Identify the blood parasite species.
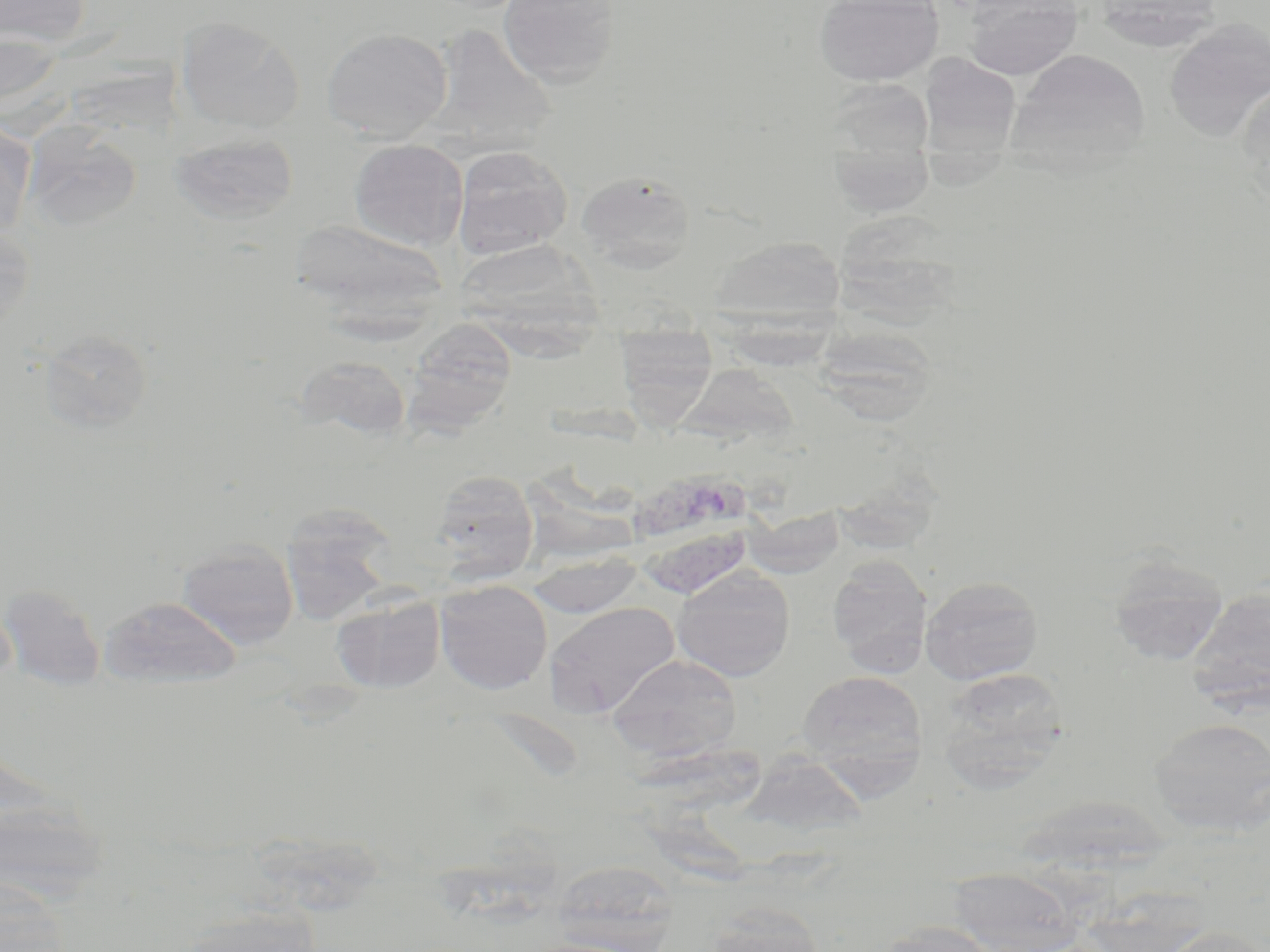

Plasmodium vivax.

{
  "field_of_view": "one of a larger specimen",
  "modality": "light microscopy",
  "stain": "May-Grünwald-Giemsa",
  "preparation": "thin blood smear",
  "uninfected_red_blood_cell_locations": "approximate bounding boxes as [x1, y1, x2, y2] in pixels: [1, 0, 93, 47], [497, 0, 621, 88], [813, 0, 944, 86], [964, 0, 1083, 80], [1093, 0, 1224, 52], [176, 16, 306, 134], [1163, 19, 1269, 142], [426, 23, 559, 156], [321, 27, 453, 142], [0, 30, 64, 119], [1008, 48, 1151, 171], [919, 53, 1021, 156], [1236, 80, 1270, 202], [0, 121, 36, 243], [25, 125, 143, 233], [167, 131, 299, 226], [349, 139, 468, 250], [829, 144, 935, 217], [452, 145, 573, 259], [576, 170, 696, 273], [839, 216, 973, 330], [290, 218, 450, 325], [0, 225, 35, 336], [708, 236, 847, 330], [467, 243, 615, 364], [402, 318, 518, 435], [614, 326, 718, 424], [812, 326, 940, 427], [38, 328, 153, 433], [292, 355, 413, 443], [693, 367, 824, 471], [429, 469, 539, 581], [279, 504, 400, 622], [745, 507, 845, 578], [176, 539, 299, 649], [526, 552, 645, 619], [1106, 552, 1230, 665], [826, 555, 931, 677], [671, 567, 796, 682], [920, 576, 1043, 685], [434, 579, 553, 695], [0, 583, 106, 691], [1184, 585, 1270, 713], [330, 592, 446, 694], [98, 594, 243, 689], [543, 601, 680, 718], [606, 654, 743, 763], [935, 668, 1070, 790], [797, 670, 928, 788], [1149, 716, 1270, 836], [549, 860, 681, 951], [948, 867, 1081, 951], [0, 874, 73, 952], [700, 904, 829, 951], [173, 906, 323, 952], [873, 920, 1001, 952], [1160, 925, 1268, 952]",
  "image_size": "1270×952 pixels",
  "magnification": "1000x",
  "plasmodium_vivax_infected_red_blood_cell_locations": "approximate bounding boxes as [x1, y1, x2, y2] in pixels: [635, 468, 761, 600]"
}